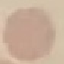

Result: no malaria parasites seen. Thin blood smear. Automatically extracted cell patch, resized to 64 × 64 pixels. Giemsa-stained preparation. Acquired by smartphone through the microscope eyepiece.